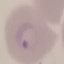
malaria status = parasitized
capture = smartphone through the microscope eyepiece
preparation = thin blood smear
stain = Giemsa
image type = automatically extracted cell patch, resized to 64 × 64 pixels